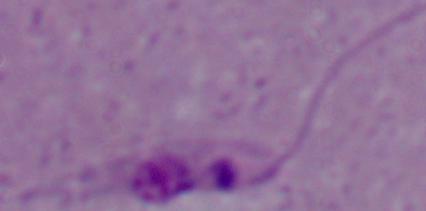

A Leishmania parasite is shown. 1000x magnification. Micrograph.